Classify this cell by malaria status.
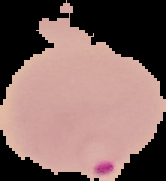

Parasitized.

Segmented cell region on a black background. From a thin blood smear. Image is 166×181 pixels.